Assess this cell for malaria.
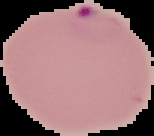
Parasitized.

Summary:
  - Preparation: thin blood smear
  - Image type: segmented cell region on a black background
  - Image size: 154×136 pixels